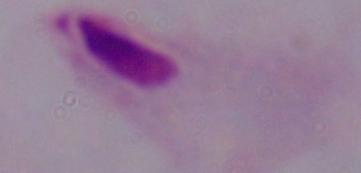
Summary:
  - Identification: trichomonad
  - Magnification: 1000x
  - Modality: micrograph